Report the malaria status of this cell.
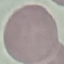
Uninfected.

Automatically extracted cell patch, resized to 64 × 64 pixels. Giemsa stain. Photographed with a smartphone camera at the microscope eyepiece. Thin blood smear.